Identify the parasite.
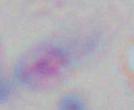
This is Toxoplasma gondii.

Summary:
  - Magnification: 1000x
  - Modality: micrograph